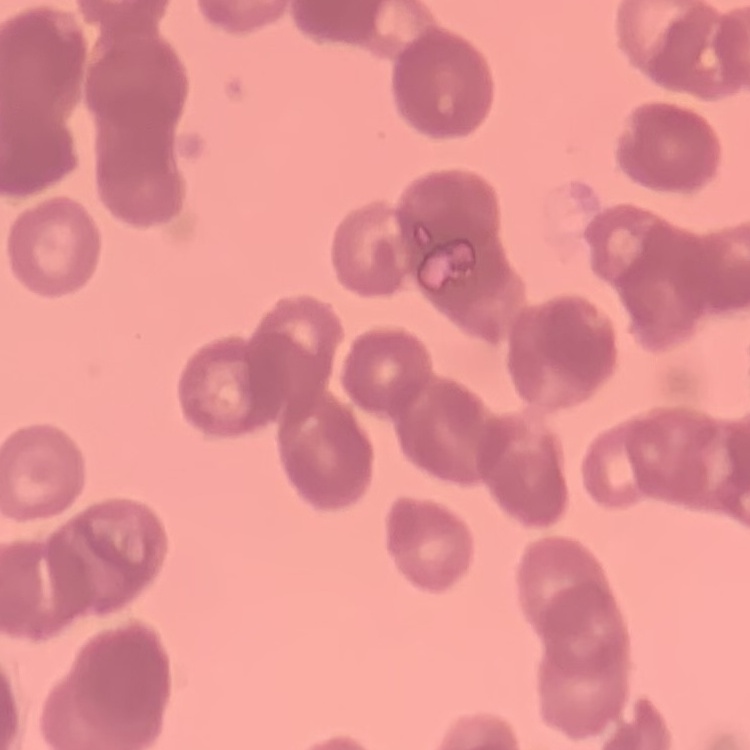
The red blood cells exhibit rouleaux formation. Thin blood smear. One tile cut from a larger photomicrograph. Field's or Giemsa stain.